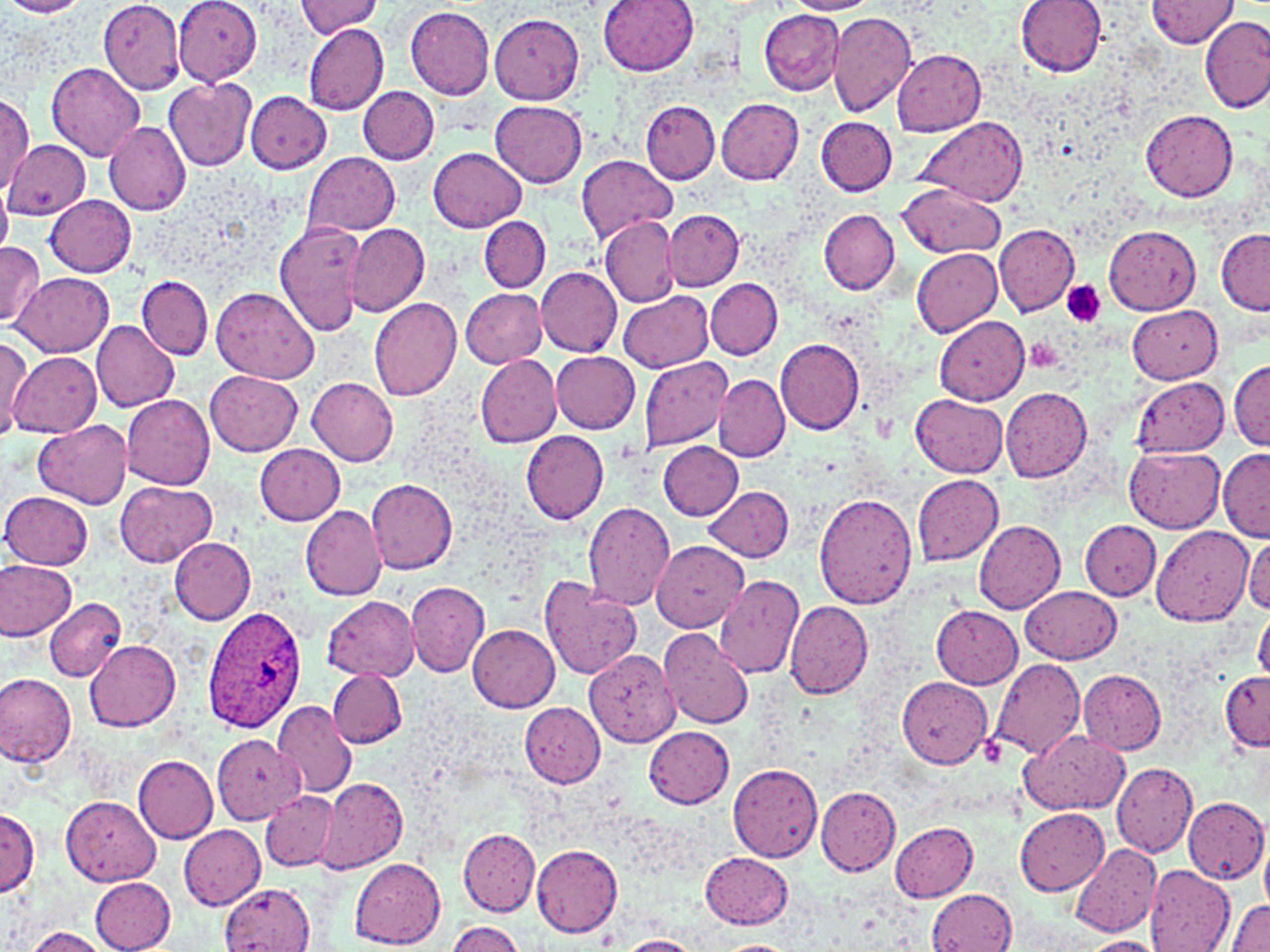 Approximate bounding boxes as named x1/y1/x2/y2 corners in pixels. Plasmodium ovale-infected red blood cell locations: (x1=202, y1=607, x2=307, y2=734). Platelet locations: (x1=1062, y1=281, x2=1106, y2=328). Uninfected red blood cell locations: (x1=0, y1=0, x2=90, y2=19), (x1=175, y1=0, x2=264, y2=85), (x1=598, y1=0, x2=699, y2=75), (x1=783, y1=0, x2=880, y2=14), (x1=1016, y1=0, x2=1105, y2=75), (x1=295, y1=1, x2=383, y2=37), (x1=1146, y1=1, x2=1238, y2=50), (x1=99, y1=2, x2=186, y2=93), (x1=404, y1=6, x2=495, y2=99), (x1=760, y1=9, x2=846, y2=95), (x1=829, y1=12, x2=916, y2=117), (x1=488, y1=13, x2=584, y2=104), (x1=1200, y1=17, x2=1270, y2=113), (x1=302, y1=22, x2=388, y2=114), (x1=893, y1=48, x2=987, y2=136), (x1=46, y1=62, x2=145, y2=161), (x1=164, y1=77, x2=256, y2=171), (x1=359, y1=86, x2=440, y2=164), (x1=243, y1=92, x2=333, y2=173), (x1=0, y1=94, x2=33, y2=191), (x1=717, y1=98, x2=804, y2=185), (x1=491, y1=101, x2=588, y2=187), (x1=641, y1=101, x2=718, y2=182), (x1=1141, y1=110, x2=1238, y2=201), (x1=816, y1=116, x2=897, y2=194), (x1=914, y1=117, x2=1027, y2=206), (x1=104, y1=120, x2=191, y2=216), (x1=2, y1=138, x2=89, y2=220), (x1=429, y1=147, x2=526, y2=231), (x1=302, y1=153, x2=401, y2=236), (x1=578, y1=155, x2=677, y2=243), (x1=898, y1=183, x2=1006, y2=257), (x1=0, y1=185, x2=13, y2=260), (x1=44, y1=193, x2=138, y2=276), (x1=819, y1=209, x2=900, y2=294), (x1=663, y1=210, x2=745, y2=290), (x1=479, y1=216, x2=550, y2=292), (x1=600, y1=217, x2=679, y2=305), (x1=274, y1=220, x2=367, y2=336), (x1=343, y1=223, x2=428, y2=315), (x1=994, y1=225, x2=1080, y2=316), (x1=1105, y1=225, x2=1200, y2=315), (x1=1216, y1=229, x2=1270, y2=315), (x1=0, y1=241, x2=42, y2=329), (x1=912, y1=249, x2=1002, y2=335), (x1=536, y1=267, x2=622, y2=356), (x1=13, y1=272, x2=113, y2=356), (x1=136, y1=275, x2=212, y2=359), (x1=705, y1=278, x2=782, y2=360), (x1=211, y1=287, x2=318, y2=385), (x1=461, y1=288, x2=547, y2=368), (x1=620, y1=290, x2=713, y2=373), (x1=368, y1=296, x2=462, y2=401), (x1=1126, y1=304, x2=1222, y2=384), (x1=932, y1=315, x2=1030, y2=405), (x1=90, y1=320, x2=180, y2=414), (x1=0, y1=337, x2=32, y2=439), (x1=775, y1=338, x2=865, y2=434), (x1=7, y1=349, x2=102, y2=437), (x1=551, y1=351, x2=641, y2=433), (x1=475, y1=353, x2=562, y2=449), (x1=638, y1=356, x2=733, y2=451), (x1=1230, y1=360, x2=1270, y2=449), (x1=206, y1=371, x2=304, y2=454), (x1=714, y1=375, x2=789, y2=462), (x1=307, y1=377, x2=399, y2=465), (x1=1134, y1=378, x2=1229, y2=455), (x1=1001, y1=387, x2=1091, y2=482), (x1=121, y1=393, x2=215, y2=489), (x1=910, y1=395, x2=1007, y2=477), (x1=33, y1=420, x2=132, y2=508), (x1=519, y1=430, x2=609, y2=523), (x1=658, y1=442, x2=743, y2=519), (x1=253, y1=443, x2=345, y2=524), (x1=1125, y1=446, x2=1224, y2=533), (x1=1217, y1=450, x2=1270, y2=541), (x1=912, y1=473, x2=1004, y2=566), (x1=116, y1=479, x2=217, y2=567), (x1=367, y1=479, x2=457, y2=575), (x1=705, y1=485, x2=794, y2=561), (x1=2, y1=491, x2=94, y2=570), (x1=813, y1=491, x2=917, y2=608), (x1=583, y1=503, x2=676, y2=610), (x1=300, y1=504, x2=388, y2=601), (x1=973, y1=520, x2=1066, y2=614), (x1=1080, y1=520, x2=1160, y2=601), (x1=1150, y1=524, x2=1255, y2=626), (x1=1245, y1=534, x2=1270, y2=616), (x1=169, y1=537, x2=257, y2=624), (x1=651, y1=540, x2=749, y2=632), (x1=0, y1=559, x2=77, y2=638), (x1=541, y1=575, x2=642, y2=680), (x1=712, y1=575, x2=803, y2=678), (x1=406, y1=581, x2=490, y2=676), (x1=1022, y1=586, x2=1121, y2=665), (x1=323, y1=596, x2=419, y2=682), (x1=43, y1=598, x2=125, y2=682), (x1=784, y1=600, x2=873, y2=701), (x1=931, y1=604, x2=1023, y2=689), (x1=1254, y1=610, x2=1270, y2=683), (x1=468, y1=625, x2=560, y2=711), (x1=659, y1=627, x2=753, y2=730), (x1=85, y1=640, x2=180, y2=732), (x1=578, y1=647, x2=681, y2=748), (x1=988, y1=658, x2=1086, y2=759), (x1=326, y1=668, x2=407, y2=748), (x1=1079, y1=669, x2=1167, y2=754), (x1=1220, y1=671, x2=1269, y2=750), (x1=0, y1=672, x2=77, y2=766), (x1=897, y1=676, x2=993, y2=768), (x1=272, y1=700, x2=356, y2=798), (x1=518, y1=701, x2=605, y2=788), (x1=644, y1=726, x2=734, y2=808), (x1=1017, y1=729, x2=1128, y2=815), (x1=213, y1=736, x2=304, y2=823), (x1=133, y1=755, x2=218, y2=842), (x1=728, y1=763, x2=822, y2=862), (x1=1112, y1=763, x2=1197, y2=857), (x1=317, y1=779, x2=407, y2=874), (x1=816, y1=787, x2=901, y2=876), (x1=259, y1=791, x2=338, y2=871), (x1=62, y1=796, x2=160, y2=885), (x1=1183, y1=797, x2=1267, y2=884), (x1=1014, y1=807, x2=1109, y2=895), (x1=0, y1=809, x2=40, y2=897), (x1=889, y1=820, x2=978, y2=900), (x1=179, y1=825, x2=266, y2=910), (x1=457, y1=826, x2=540, y2=915), (x1=1260, y1=836, x2=1270, y2=916), (x1=1071, y1=843, x2=1161, y2=936), (x1=532, y1=844, x2=623, y2=936), (x1=700, y1=852, x2=793, y2=928), (x1=350, y1=858, x2=446, y2=948), (x1=1144, y1=865, x2=1235, y2=951), (x1=89, y1=876, x2=176, y2=952), (x1=221, y1=884, x2=314, y2=952), (x1=926, y1=889, x2=1016, y2=952), (x1=1227, y1=900, x2=1270, y2=952), (x1=445, y1=921, x2=526, y2=952), (x1=24, y1=926, x2=115, y2=952), (x1=616, y1=935, x2=703, y2=952), (x1=1080, y1=937, x2=1164, y2=952), (x1=712, y1=940, x2=797, y2=951). Slide-level diagnosis: Plasmodium ovale. Optical microscopy. Image is 1270×952 pixels. May-Grünwald-Giemsa-stained preparation. Captured at 1000x magnification. Thin blood smear. Single field of view.